Assess the morphology of the erythrocytes.
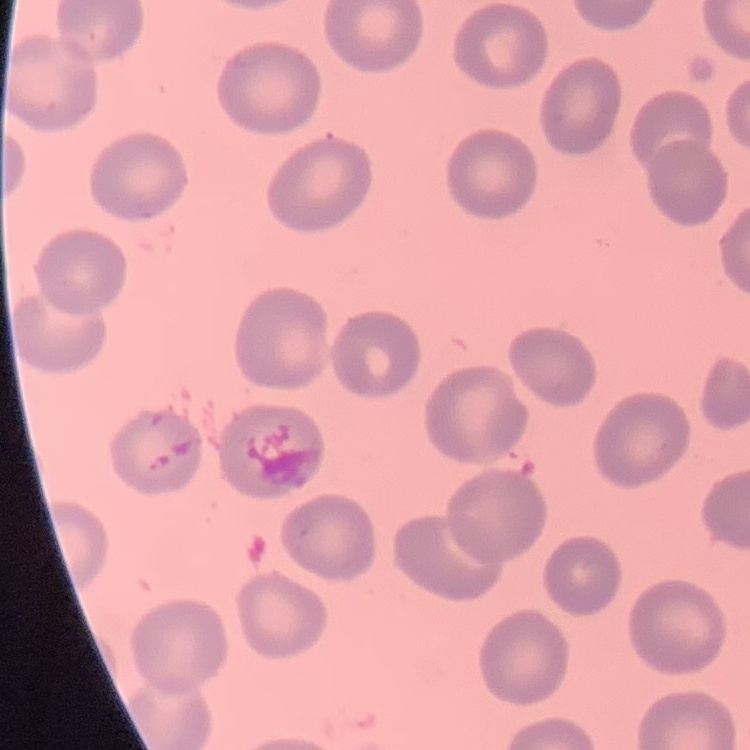
No rouleaux formation.

stain = Field's or Giemsa
image type = one tile cut from a larger photomicrograph
preparation = thin blood smear